Report the malaria status of this cell.
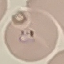
It is parasitized.

Summary:
  - Preparation: thin blood film
  - Capture: smartphone through the microscope eyepiece
  - Image type: cell patch, automatically extracted from a larger field of view and resized to 64 × 64 pixels
  - Stain: Giemsa